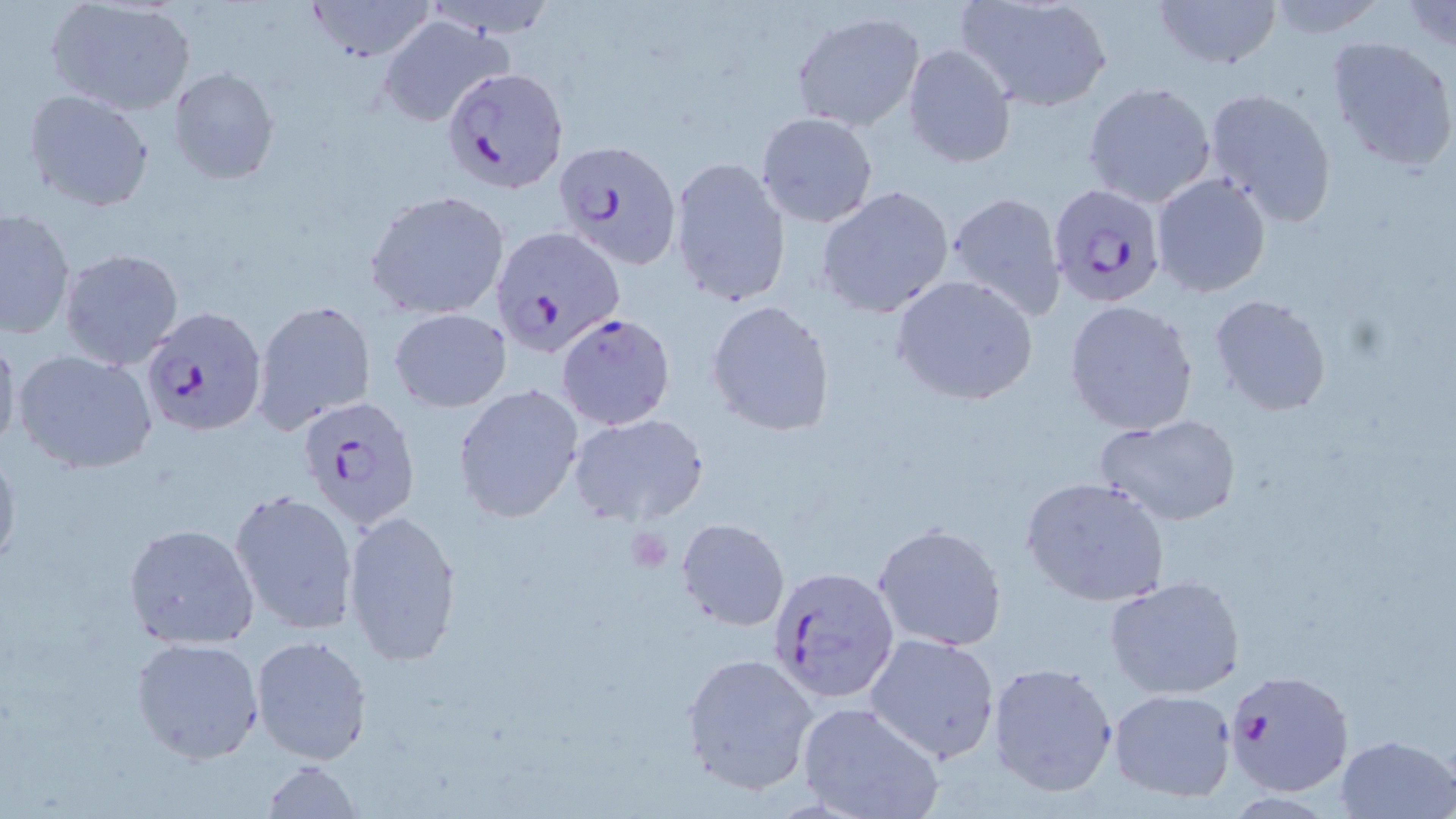

slide_level_diagnosis: Plasmodium falciparum
uninfected_red_blood_cell_locations: 'approximate bounding boxes as (x1,y1)-(x2,y2) corner pairs in pixels: (45,0)-(196,117), (305,0)-(438,62), (1150,0)-(1284,73), (952,1)-(1114,113), (1263,1)-(1391,38), (1397,1)-(1456,55), (790,10)-(926,133), (378,15)-(513,126), (1324,34)-(1456,175), (902,44)-(1016,167), (169,67)-(280,186), (1082,81)-(1218,207), (1203,85)-(1338,226), (23,90)-(155,212), (756,111)-(879,228), (668,157)-(789,308), (1151,174)-(1270,296), (816,187)-(955,318), (364,190)-(512,321), (942,190)-(1069,323), (1,208)-(76,340), (58,248)-(185,372), (890,273)-(1039,406), (1207,294)-(1332,418), (1064,299)-(1200,435), (253,300)-(376,434), (706,301)-(834,435), (390,308)-(511,412), (0,325)-(22,460), (11,347)-(160,475), (452,383)-(585,524), (568,413)-(711,527), (1096,413)-(1242,527), (0,441)-(22,575), (1019,476)-(1172,606), (230,490)-(359,637), (341,508)-(462,667), (676,518)-(790,632), (123,523)-(261,648), (873,523)-(1006,650), (1104,575)-(1245,700), (864,632)-(1001,764), (250,634)-(372,765), (130,635)-(264,764), (680,652)-(821,797), (986,662)-(1120,799), (1108,688)-(1237,802), (796,701)-(946,819), (1335,733)-(1455,819), (263,758)-(363,818)'
magnification: 1000x
platelet_locations: 'approximate bounding boxes as (x1,y1)-(x2,y2) corner pairs in pixels: (624,526)-(673,574)'
preparation: thin blood smear
plasmodium_falciparum_infected_red_blood_cell_locations: 'approximate bounding boxes as (x1,y1)-(x2,y2) corner pairs in pixels: (441,66)-(570,197), (554,138)-(683,268), (1047,182)-(1167,306), (493,228)-(627,357), (140,306)-(268,436), (556,314)-(675,431), (295,400)-(421,533), (767,565)-(900,706), (1225,669)-(1353,796)'
modality: optical microscopy
field_of_view: single
stain: May-Grünwald-Giemsa
image_size: 1456×819 pixels